Report the malaria status of this cell.
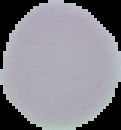
Uninfected.

image size = 121×130 pixels
preparation = thin blood smear
image type = segmented cell region on a black background